Give the extent of all Plasmodium falciparum-infected red blood cells.
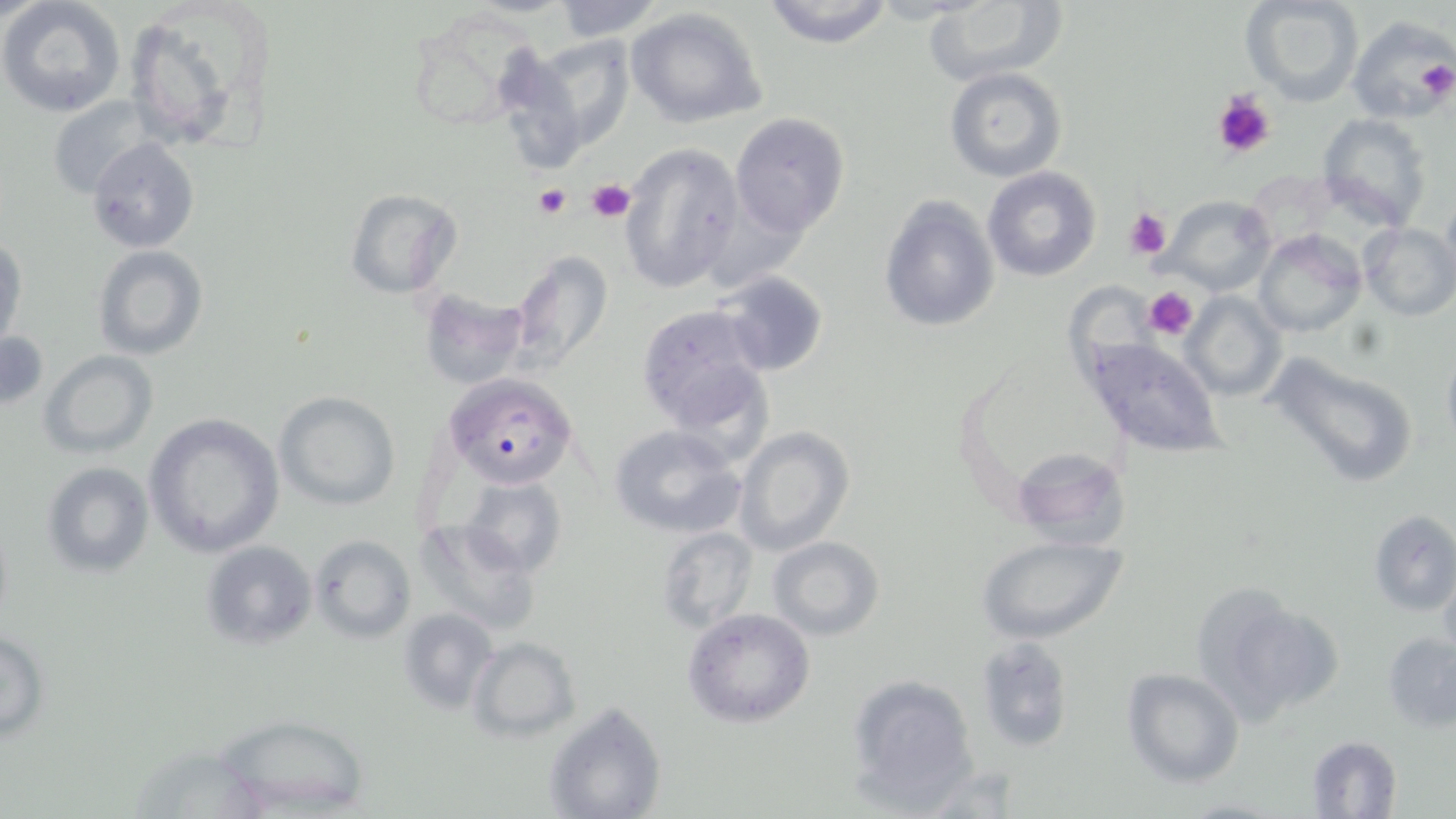

Approximate bounding boxes as [x1, y1, x2, y2] in pixels.
Plasmodium falciparum-infected red blood cells: [0, 332, 51, 408], [443, 373, 577, 490].

Platelet locations: [1414, 58, 1454, 102], [1212, 91, 1277, 160], [587, 179, 636, 223], [533, 185, 571, 221], [1123, 208, 1171, 260], [1142, 286, 1199, 341]. Uninfected red blood cell locations: [0, 0, 127, 117], [550, 0, 665, 41], [760, 0, 895, 48], [1240, 0, 1364, 106], [923, 1, 1064, 86], [120, 3, 275, 154], [625, 7, 768, 128], [1347, 15, 1456, 124], [518, 34, 635, 158], [945, 68, 1067, 184], [47, 94, 156, 199], [730, 113, 851, 238], [1316, 113, 1432, 226], [85, 138, 200, 255], [620, 142, 742, 293], [982, 166, 1102, 282], [343, 187, 463, 299], [1442, 192, 1456, 289], [1163, 195, 1274, 294], [878, 196, 1000, 332], [1358, 221, 1456, 321], [1253, 230, 1366, 339], [0, 235, 26, 347], [94, 246, 208, 362], [507, 251, 615, 373], [716, 270, 829, 375], [418, 287, 529, 389], [1180, 292, 1287, 401], [637, 305, 769, 433], [1083, 338, 1223, 457], [1441, 343, 1456, 450], [1261, 349, 1420, 489], [40, 350, 159, 459], [274, 391, 401, 512], [143, 413, 285, 557], [606, 423, 747, 539], [732, 426, 853, 555], [1010, 446, 1132, 548], [42, 463, 155, 579], [459, 475, 568, 576], [1367, 509, 1456, 616], [415, 517, 544, 639], [655, 526, 758, 635], [976, 534, 1126, 644], [309, 535, 418, 643], [769, 535, 885, 640], [201, 540, 317, 651], [1439, 563, 1456, 662], [1193, 589, 1337, 725], [683, 607, 816, 728], [399, 608, 498, 714], [0, 625, 50, 746], [1383, 631, 1456, 733], [468, 637, 578, 742], [976, 638, 1079, 753], [1123, 668, 1246, 787], [846, 674, 982, 810], [543, 701, 668, 819], [208, 712, 376, 817], [1304, 734, 1404, 819]. Slide-level diagnosis: Plasmodium falciparum. Image is 1456×819 pixels. May-Grünwald-Giemsa-stained preparation. 1000x magnification. Thin blood film. One field of a larger specimen. Optical microscopy.